State which parasite is depicted.
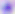

Toxoplasma gondii.

Photomicrograph. 400x magnification.